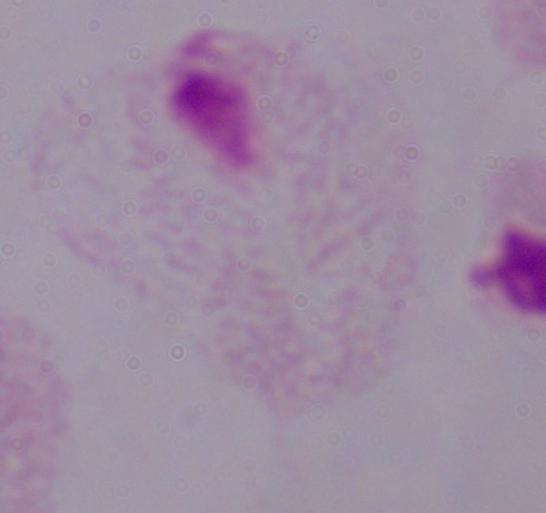

identification: trichomonad
magnification: 1000x
modality: micrograph